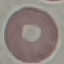

Summary:
  - Malaria status: uninfected
  - Capture: smartphone through the microscope eyepiece
  - Image type: automatically extracted cell patch, resized to 64 × 64 pixels
  - Stain: Giemsa
  - Preparation: thin blood film